Classify this cell by malaria status.
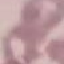
It is uninfected.

Thin blood film. Photographed with a smartphone camera at the microscope eyepiece. Giemsa stain. Automatically extracted cell patch, resized to 64 × 64 pixels.